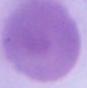

{
  "identification": "red blood cell",
  "magnification": "1000x",
  "modality": "photomicrograph"
}